Assess for Plasmodium parasites.
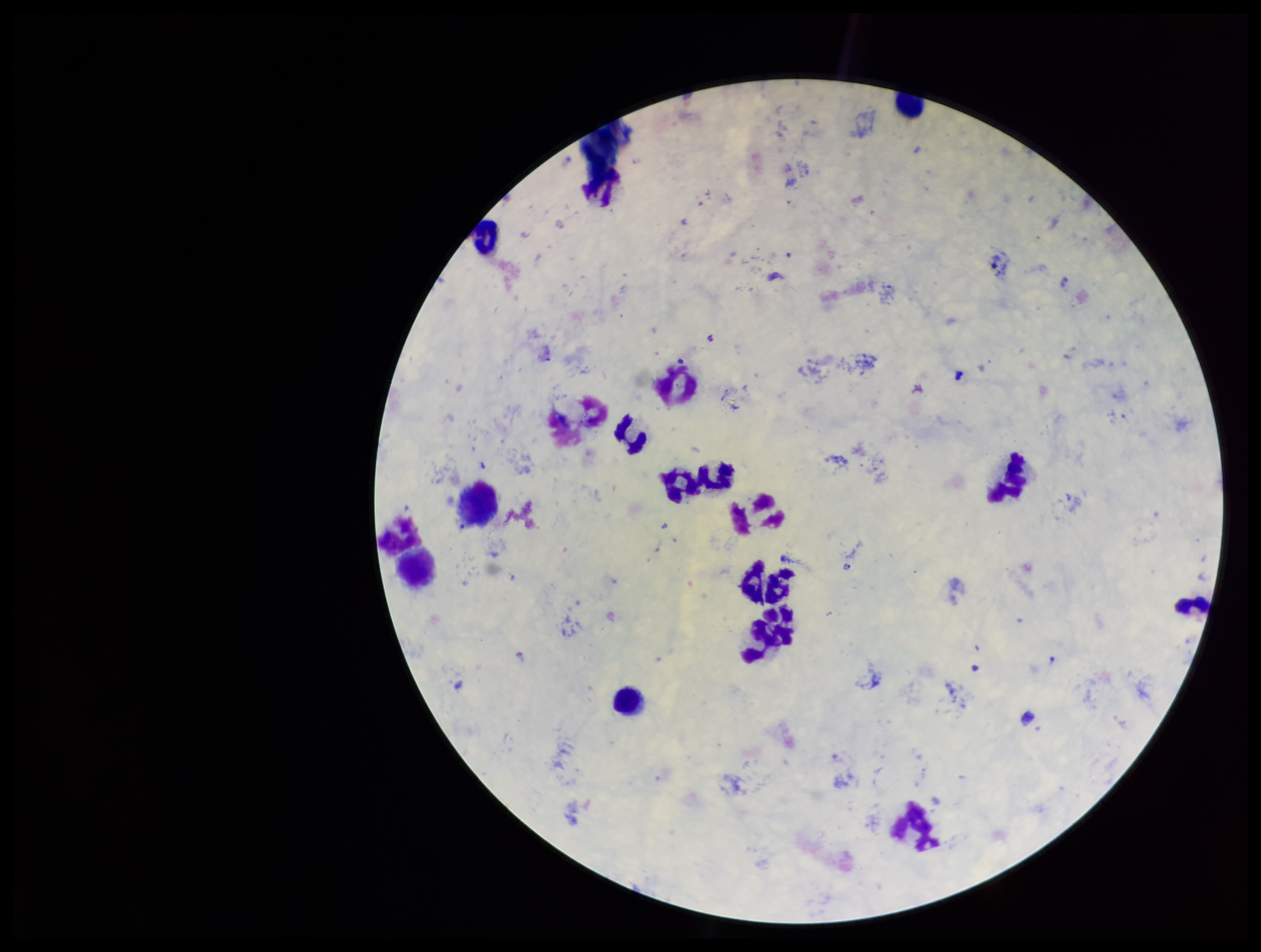
Seen.

Smartphone photograph taken through the eyepiece of a microscope. Stained with Giemsa. Parasite count: 1. Image is 1261×952 pixels. Preparation: thick smear. Patient malaria status: positive. One field from this slide. Species reported for this patient: Plasmodium vivax. Leukocyte count: 15.